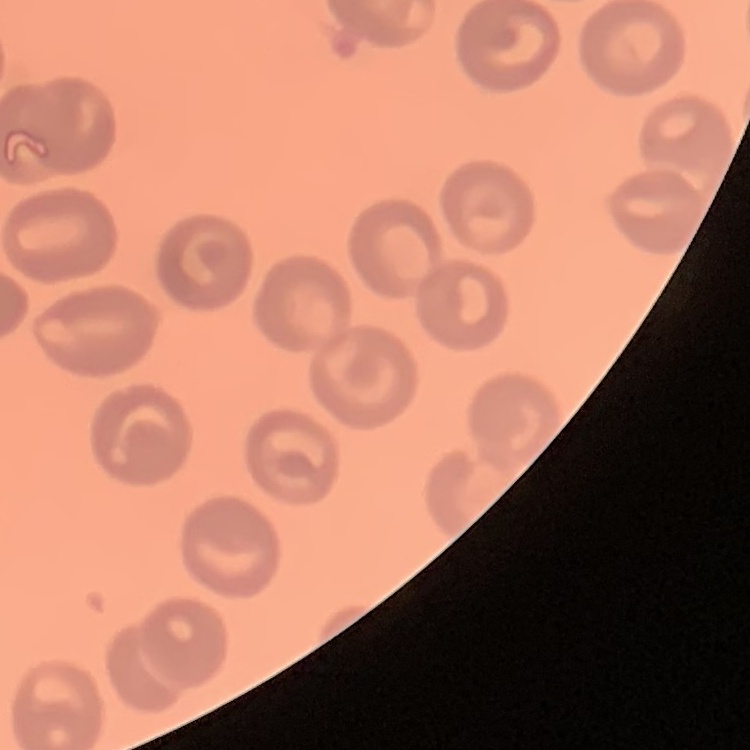

Summary:
  - Red blood cell morphology: no rouleaux formation
  - Stain: Field's or Giemsa
  - Image type: square crop of a larger photomicrograph
  - Preparation: thin peripheral smear